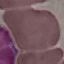
Malaria status: uninfected. Automatically extracted cell patch, resized to 64 × 64 pixels. Acquired by smartphone through the microscope eyepiece. Thin smear of blood. Giemsa stain.